Give the extent of all Plasmodium ovale-infected red blood cells.
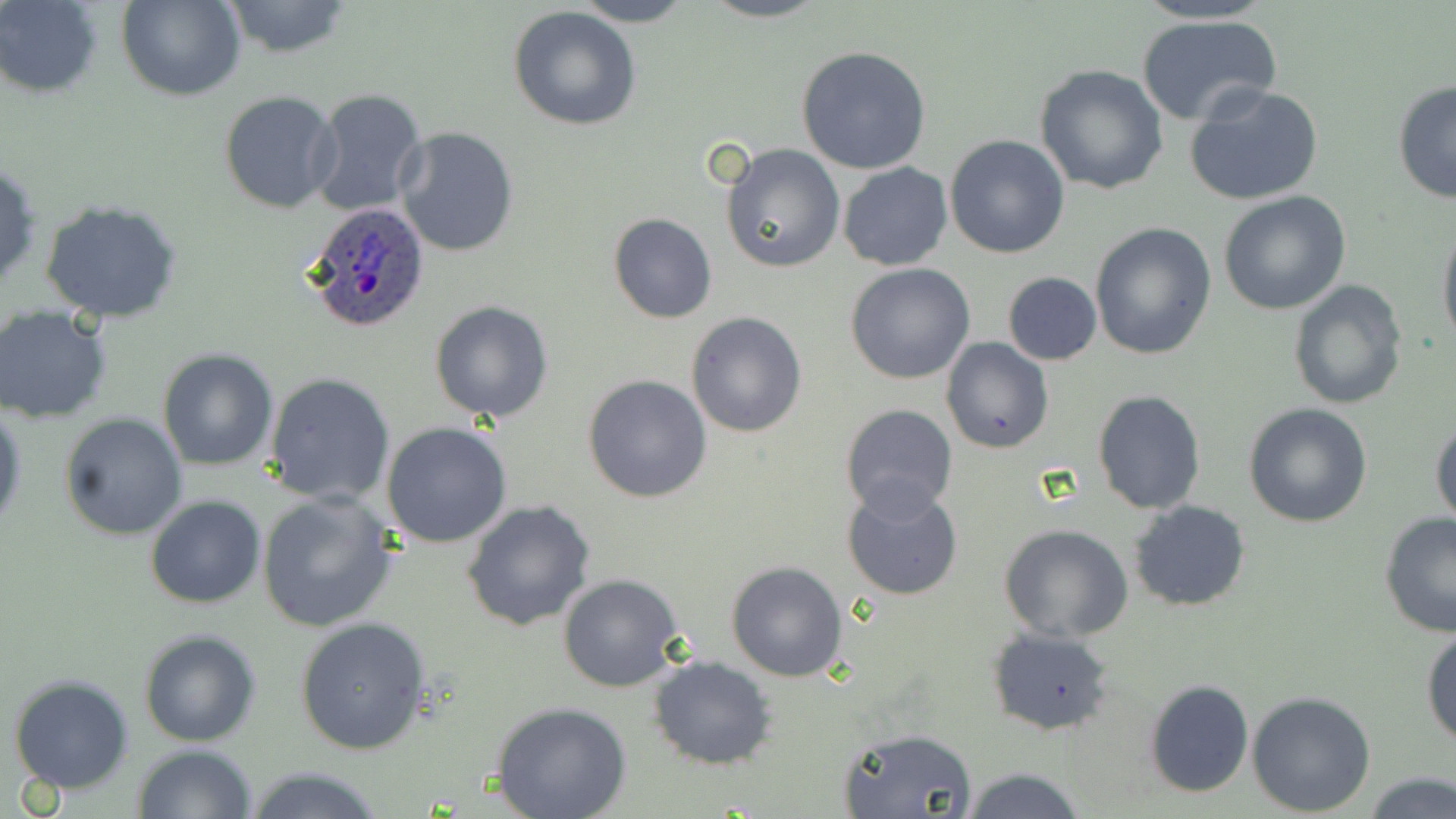
Approximate bounding boxes as named x1/y1/x2/y2 corners in pixels.
Plasmodium ovale-infected red blood cells: (x1=303, y1=202, x2=430, y2=332).

Uninfected red blood cell locations: (x1=0, y1=0, x2=103, y2=98), (x1=117, y1=0, x2=244, y2=101), (x1=574, y1=0, x2=696, y2=27), (x1=699, y1=0, x2=827, y2=23), (x1=1129, y1=0, x2=1276, y2=25), (x1=221, y1=1, x2=352, y2=57), (x1=509, y1=7, x2=643, y2=131), (x1=1134, y1=13, x2=1282, y2=126), (x1=795, y1=45, x2=932, y2=175), (x1=1034, y1=63, x2=1169, y2=194), (x1=1392, y1=81, x2=1455, y2=204), (x1=1183, y1=84, x2=1323, y2=206), (x1=308, y1=88, x2=428, y2=218), (x1=219, y1=90, x2=343, y2=213), (x1=395, y1=125, x2=520, y2=257), (x1=944, y1=134, x2=1070, y2=259), (x1=721, y1=143, x2=845, y2=272), (x1=0, y1=156, x2=41, y2=296), (x1=837, y1=162, x2=954, y2=271), (x1=1217, y1=191, x2=1350, y2=315), (x1=39, y1=198, x2=185, y2=322), (x1=608, y1=213, x2=717, y2=324), (x1=1437, y1=221, x2=1456, y2=349), (x1=1090, y1=223, x2=1218, y2=360), (x1=845, y1=263, x2=976, y2=384), (x1=1002, y1=271, x2=1102, y2=366), (x1=1289, y1=278, x2=1407, y2=409), (x1=430, y1=300, x2=556, y2=422), (x1=0, y1=311, x2=113, y2=424), (x1=686, y1=311, x2=807, y2=437), (x1=941, y1=338, x2=1054, y2=454), (x1=157, y1=344, x2=276, y2=469), (x1=263, y1=372, x2=396, y2=506), (x1=582, y1=374, x2=712, y2=503), (x1=1091, y1=389, x2=1208, y2=514), (x1=0, y1=403, x2=25, y2=537), (x1=839, y1=403, x2=960, y2=519), (x1=1242, y1=403, x2=1373, y2=528), (x1=60, y1=413, x2=188, y2=540), (x1=1429, y1=416, x2=1455, y2=529), (x1=381, y1=422, x2=513, y2=548), (x1=841, y1=484, x2=965, y2=602), (x1=256, y1=491, x2=399, y2=633), (x1=145, y1=496, x2=265, y2=607), (x1=463, y1=498, x2=596, y2=632), (x1=1129, y1=500, x2=1251, y2=611), (x1=1379, y1=512, x2=1456, y2=638), (x1=998, y1=522, x2=1134, y2=642), (x1=726, y1=561, x2=849, y2=682), (x1=559, y1=573, x2=686, y2=693), (x1=295, y1=617, x2=431, y2=754), (x1=1421, y1=626, x2=1455, y2=748), (x1=986, y1=628, x2=1114, y2=736), (x1=140, y1=630, x2=263, y2=747), (x1=648, y1=656, x2=777, y2=769), (x1=7, y1=672, x2=135, y2=794), (x1=1143, y1=679, x2=1255, y2=799), (x1=1245, y1=690, x2=1377, y2=816), (x1=490, y1=703, x2=631, y2=819), (x1=837, y1=727, x2=978, y2=819), (x1=133, y1=744, x2=256, y2=819), (x1=240, y1=765, x2=389, y2=819), (x1=960, y1=765, x2=1089, y2=819), (x1=1361, y1=770, x2=1456, y2=819). Slide-level diagnosis: Plasmodium ovale. Optical microscopy. May-Grünwald-Giemsa stain. Thin blood film. Captured at 1000x magnification. Image is 1456×819 pixels. Single field of view.